Identify the blood parasite species.
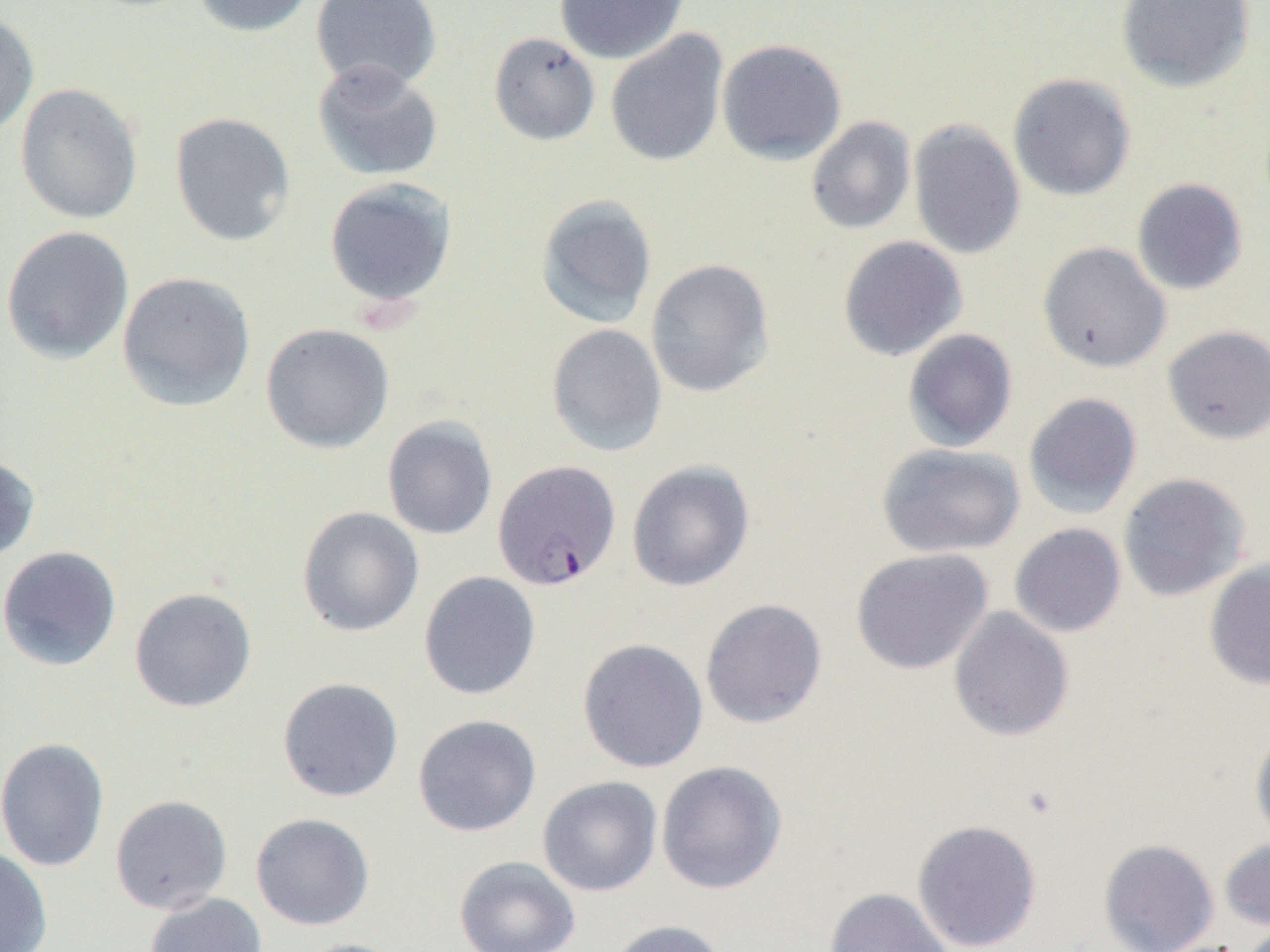

Plasmodium falciparum.

Summary:
  - Coordinate format: approximate bounding boxes as [x1, y1, x2, y2] in pixels
  - Uninfected red blood cell locations: [192, 0, 315, 37], [310, 0, 442, 93], [554, 0, 689, 64], [1116, 0, 1256, 93], [0, 11, 39, 140], [604, 30, 729, 167], [488, 31, 600, 146], [716, 38, 847, 165], [312, 60, 443, 182], [1007, 73, 1136, 202], [14, 82, 144, 225], [169, 111, 296, 247], [805, 116, 916, 235], [908, 119, 1026, 260], [323, 177, 458, 309], [1131, 178, 1248, 295], [534, 194, 657, 329], [0, 225, 134, 364], [837, 235, 968, 362], [1037, 241, 1171, 373], [645, 258, 775, 398], [117, 271, 256, 412], [260, 323, 394, 454], [546, 323, 667, 457], [1162, 325, 1270, 444], [902, 328, 1018, 453], [1023, 392, 1142, 518], [382, 416, 498, 540], [876, 442, 1025, 558], [0, 454, 40, 562], [626, 460, 755, 591], [1118, 472, 1251, 601], [296, 506, 424, 637], [1009, 523, 1127, 638], [0, 545, 121, 671], [851, 548, 994, 675], [1203, 559, 1270, 691], [418, 571, 541, 700], [129, 586, 257, 713], [700, 598, 828, 729], [948, 606, 1075, 742], [577, 638, 708, 773], [277, 677, 403, 802], [412, 714, 541, 837], [1250, 725, 1270, 848], [0, 737, 110, 872], [656, 760, 787, 894], [537, 776, 662, 896], [110, 794, 233, 914], [250, 812, 374, 930], [911, 819, 1042, 951], [1220, 837, 1270, 932], [1098, 838, 1219, 952], [0, 847, 52, 952], [454, 855, 581, 952], [825, 886, 953, 952], [144, 892, 267, 952], [606, 919, 729, 952], [291, 938, 408, 952]
  - Plasmodium falciparum-infected red blood cell locations: [492, 459, 621, 590]
  - Modality: light microscopy
  - Magnification: 1000x
  - Image size: 1270×952 pixels
  - Field of view: one of a larger specimen
  - Preparation: thin blood smear